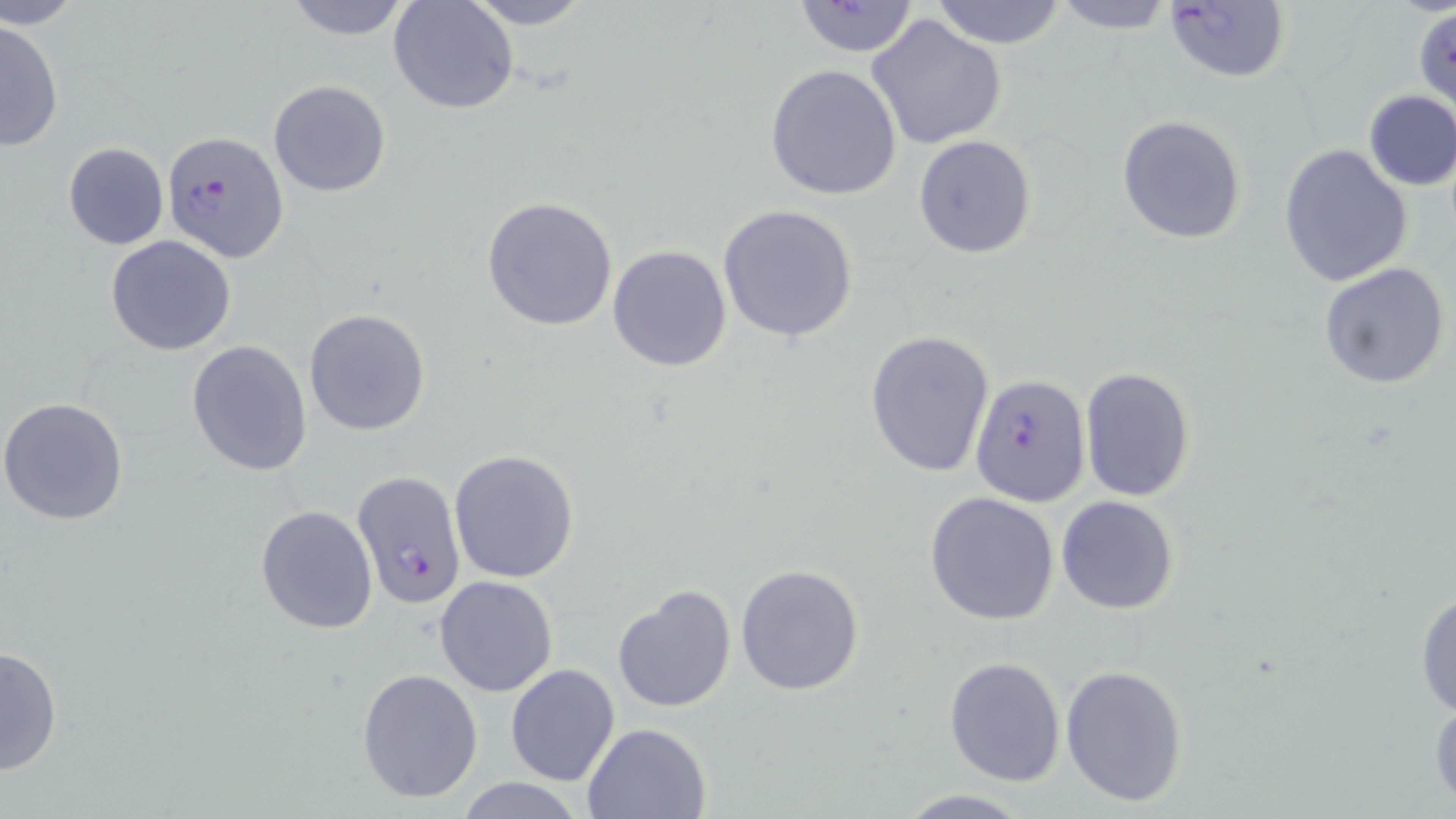

Summary:
  - Coordinate format: approximate bounding boxes as (x1, y1, x2, y2) in pixels
  - Plasmodium falciparum-infected red blood cell locations: (163, 132, 289, 263), (969, 374, 1091, 505), (353, 472, 466, 611)
  - Uninfected red blood cell locations: (3, 0, 89, 29), (279, 0, 416, 41), (460, 0, 596, 29), (930, 0, 1068, 48), (1052, 0, 1174, 33), (1161, 0, 1289, 84), (389, 1, 519, 116), (789, 2, 924, 57), (1412, 10, 1456, 110), (864, 13, 1009, 151), (0, 19, 65, 153), (765, 63, 903, 200), (268, 79, 390, 198), (1361, 90, 1455, 191), (1117, 115, 1246, 245), (912, 135, 1037, 259), (62, 141, 170, 250), (1278, 144, 1412, 287), (481, 196, 618, 332), (718, 204, 858, 343), (105, 235, 237, 356), (607, 244, 731, 372), (1319, 262, 1450, 390), (303, 308, 431, 437), (866, 329, 996, 478), (186, 338, 313, 476), (1080, 366, 1196, 501), (1, 396, 130, 524), (447, 447, 580, 583), (923, 492, 1062, 627), (1055, 495, 1180, 614), (255, 505, 379, 633), (735, 562, 865, 697), (434, 574, 560, 696), (1414, 582, 1456, 722), (612, 585, 737, 714), (1, 644, 63, 776), (943, 657, 1066, 787), (1061, 663, 1188, 804), (505, 664, 621, 786), (356, 668, 484, 803), (1428, 690, 1456, 811), (582, 721, 712, 818), (454, 776, 587, 818), (896, 789, 1034, 818)
  - Slide-level diagnosis: Plasmodium falciparum
  - Magnification: 1000x
  - Modality: optical microscopy
  - Field of view: single
  - Image size: 1456×819 pixels
  - Preparation: thin blood film
  - Stain: May-Grünwald-Giemsa